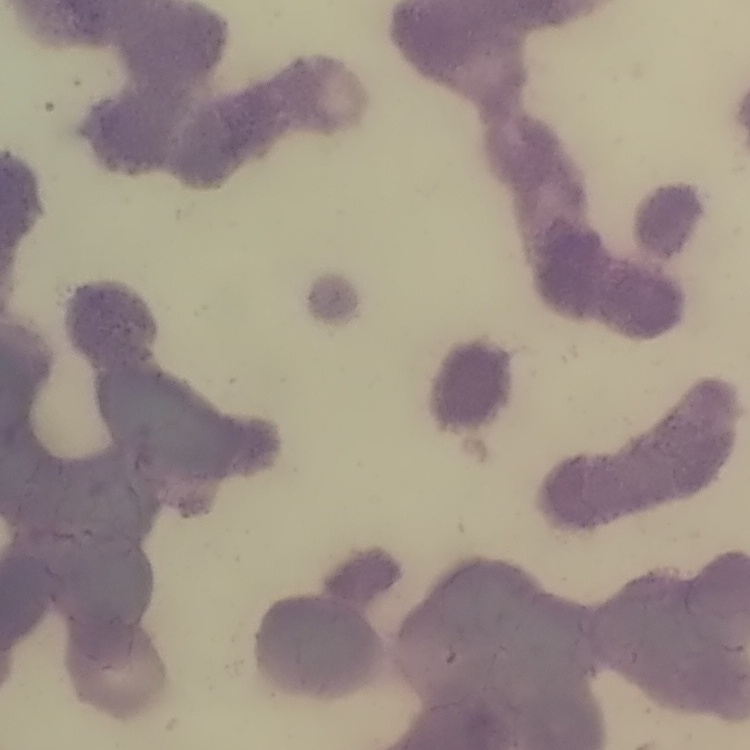

Summary:
  - Erythrocyte morphology: rouleaux formation
  - Preparation: thin blood film
  - Stain: Field's or Giemsa
  - Image type: square crop of a larger photomicrograph